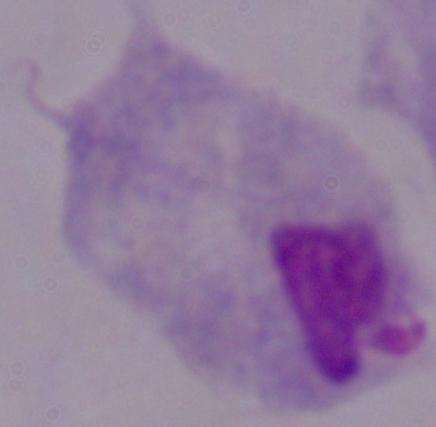

modality = photomicrograph
magnification = 1000x
identification = trichomonad